Describe the morphology of the erythrocytes.
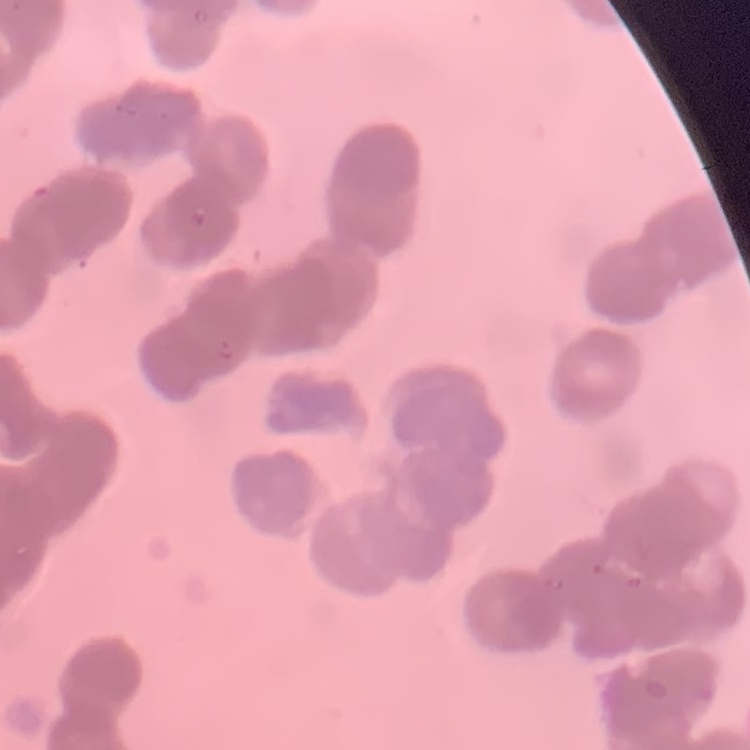

They show rouleaux formation.

{
  "image_type": "one tile cut from a larger photomicrograph",
  "preparation": "thin blood smear",
  "stain": "Field's or Giemsa"
}